Assess this cell for malaria.
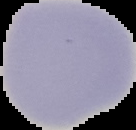
Uninfected.

Image is 136×130 pixels. From a thin blood film. The area outside the segmented cell region is set to black.